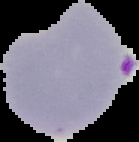

{
  "image_size": "139×142 pixels",
  "image_type": "cell region segmented out of the field of view; surrounding area masked to black",
  "result": "Plasmodium parasites detected",
  "preparation": "thin blood film"
}